Assess this cell for malaria.
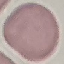
It is uninfected.

Automatically extracted cell patch, resized to 64 × 64 pixels. Thin blood film. Giemsa stain. Photographed with a smartphone camera at the microscope eyepiece.